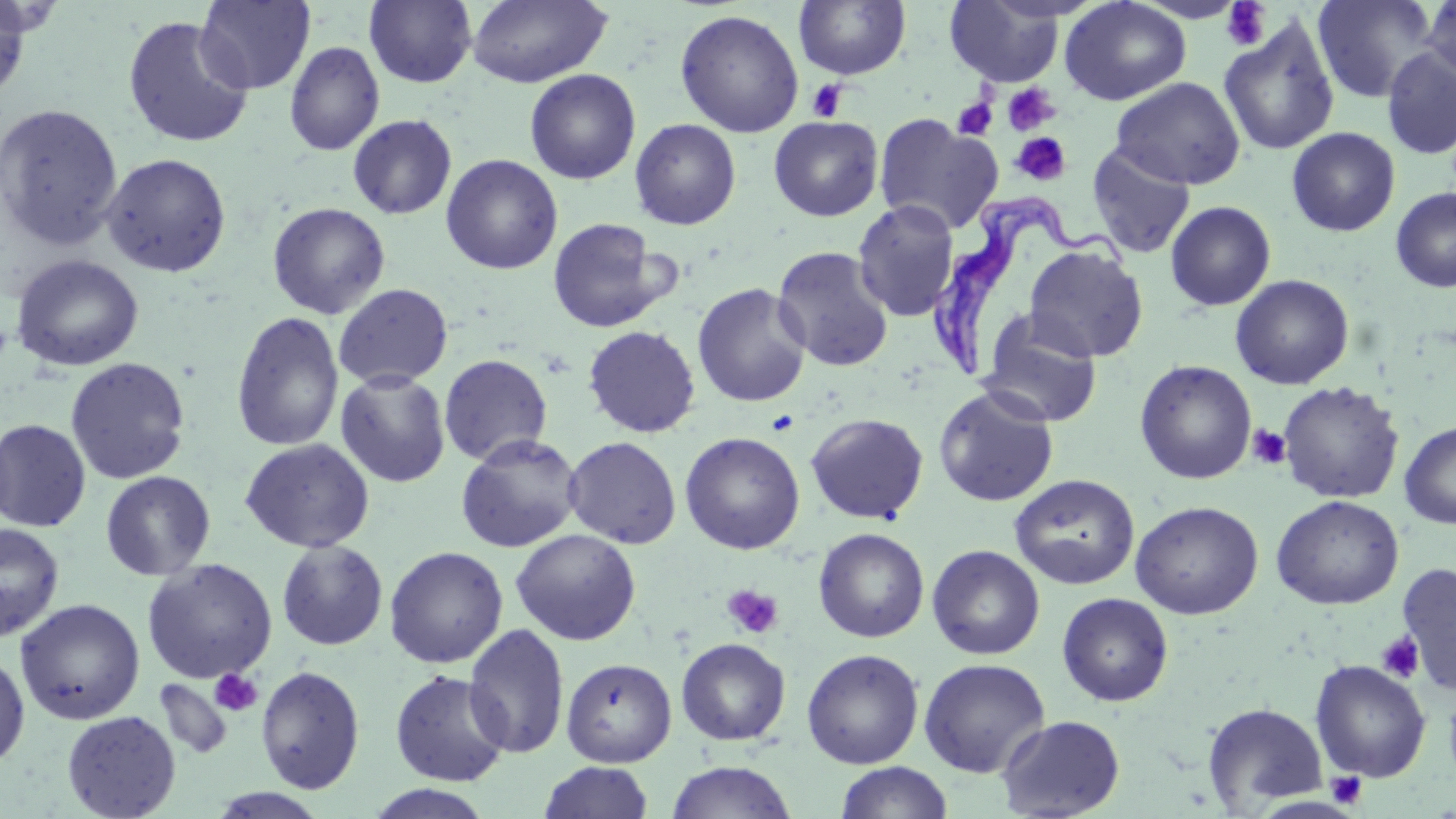
Summary:
  - Coordinate format: approximate bounding boxes as named x1/y1/x2/y2 corners in pixels
  - Trypanosoma brucei locations: (x1=922, y1=192, x2=1138, y2=377)
  - Platelet locations: (x1=1220, y1=2, x2=1272, y2=52), (x1=807, y1=79, x2=849, y2=122), (x1=1002, y1=84, x2=1059, y2=135), (x1=952, y1=97, x2=998, y2=140), (x1=1010, y1=132, x2=1071, y2=186), (x1=766, y1=410, x2=801, y2=436), (x1=1247, y1=424, x2=1291, y2=470), (x1=722, y1=584, x2=784, y2=639), (x1=1376, y1=632, x2=1425, y2=683), (x1=209, y1=669, x2=263, y2=716), (x1=1326, y1=771, x2=1367, y2=808)
  - Uninfected red blood cell locations: (x1=0, y1=0, x2=32, y2=102), (x1=196, y1=0, x2=316, y2=94), (x1=364, y1=0, x2=477, y2=88), (x1=467, y1=0, x2=612, y2=88), (x1=1059, y1=0, x2=1192, y2=105), (x1=1311, y1=0, x2=1442, y2=103), (x1=1420, y1=0, x2=1455, y2=89), (x1=793, y1=1, x2=911, y2=80), (x1=944, y1=1, x2=1066, y2=87), (x1=674, y1=9, x2=804, y2=138), (x1=122, y1=15, x2=255, y2=149), (x1=1219, y1=15, x2=1340, y2=157), (x1=285, y1=41, x2=384, y2=156), (x1=1380, y1=45, x2=1456, y2=160), (x1=524, y1=68, x2=641, y2=185), (x1=1111, y1=77, x2=1246, y2=190), (x1=0, y1=103, x2=123, y2=250), (x1=348, y1=114, x2=457, y2=220), (x1=874, y1=114, x2=1002, y2=233), (x1=769, y1=116, x2=883, y2=221), (x1=630, y1=118, x2=741, y2=230), (x1=1286, y1=127, x2=1400, y2=236), (x1=1086, y1=143, x2=1196, y2=258), (x1=101, y1=153, x2=231, y2=277), (x1=441, y1=154, x2=563, y2=275), (x1=1391, y1=187, x2=1456, y2=293), (x1=852, y1=200, x2=961, y2=321), (x1=1165, y1=201, x2=1276, y2=311), (x1=267, y1=202, x2=391, y2=319), (x1=547, y1=217, x2=673, y2=333), (x1=1024, y1=244, x2=1148, y2=363), (x1=772, y1=246, x2=895, y2=373), (x1=10, y1=254, x2=144, y2=372), (x1=1230, y1=274, x2=1354, y2=389), (x1=333, y1=283, x2=453, y2=390), (x1=691, y1=283, x2=811, y2=407), (x1=231, y1=311, x2=344, y2=452), (x1=976, y1=311, x2=1103, y2=427), (x1=582, y1=325, x2=701, y2=437), (x1=439, y1=354, x2=553, y2=466), (x1=65, y1=357, x2=191, y2=484), (x1=1134, y1=360, x2=1257, y2=484), (x1=335, y1=371, x2=451, y2=487), (x1=1277, y1=380, x2=1404, y2=503), (x1=933, y1=386, x2=1059, y2=507), (x1=806, y1=413, x2=928, y2=524), (x1=0, y1=420, x2=91, y2=532), (x1=1399, y1=420, x2=1456, y2=529), (x1=680, y1=431, x2=805, y2=554), (x1=455, y1=434, x2=583, y2=553), (x1=563, y1=436, x2=682, y2=549), (x1=240, y1=438, x2=375, y2=553), (x1=100, y1=471, x2=215, y2=581), (x1=1009, y1=474, x2=1139, y2=590), (x1=1271, y1=495, x2=1403, y2=610), (x1=1130, y1=500, x2=1264, y2=619), (x1=0, y1=522, x2=65, y2=643), (x1=813, y1=527, x2=929, y2=643), (x1=510, y1=528, x2=641, y2=645), (x1=276, y1=540, x2=388, y2=651), (x1=927, y1=544, x2=1045, y2=660), (x1=384, y1=546, x2=508, y2=668), (x1=142, y1=558, x2=277, y2=683), (x1=1395, y1=562, x2=1456, y2=693), (x1=1057, y1=592, x2=1173, y2=706), (x1=14, y1=598, x2=145, y2=725), (x1=463, y1=623, x2=570, y2=759), (x1=676, y1=637, x2=791, y2=745), (x1=801, y1=649, x2=924, y2=769), (x1=0, y1=650, x2=30, y2=768), (x1=561, y1=658, x2=677, y2=767), (x1=918, y1=658, x2=1050, y2=778), (x1=1310, y1=660, x2=1431, y2=782), (x1=256, y1=664, x2=365, y2=794), (x1=389, y1=669, x2=511, y2=787), (x1=154, y1=678, x2=233, y2=761), (x1=1203, y1=701, x2=1328, y2=812), (x1=62, y1=710, x2=181, y2=819), (x1=996, y1=715, x2=1126, y2=818), (x1=665, y1=760, x2=797, y2=819), (x1=538, y1=761, x2=654, y2=819), (x1=835, y1=762, x2=954, y2=819), (x1=361, y1=785, x2=497, y2=819), (x1=207, y1=788, x2=331, y2=818)
  - Slide-level diagnosis: Trypanosoma brucei
  - Stain: May-Grünwald-Giemsa
  - Preparation: thin blood film
  - Magnification: 1000x
  - Modality: light microscopy
  - Field of view: single
  - Image size: 1456×819 pixels